State the blood parasite species.
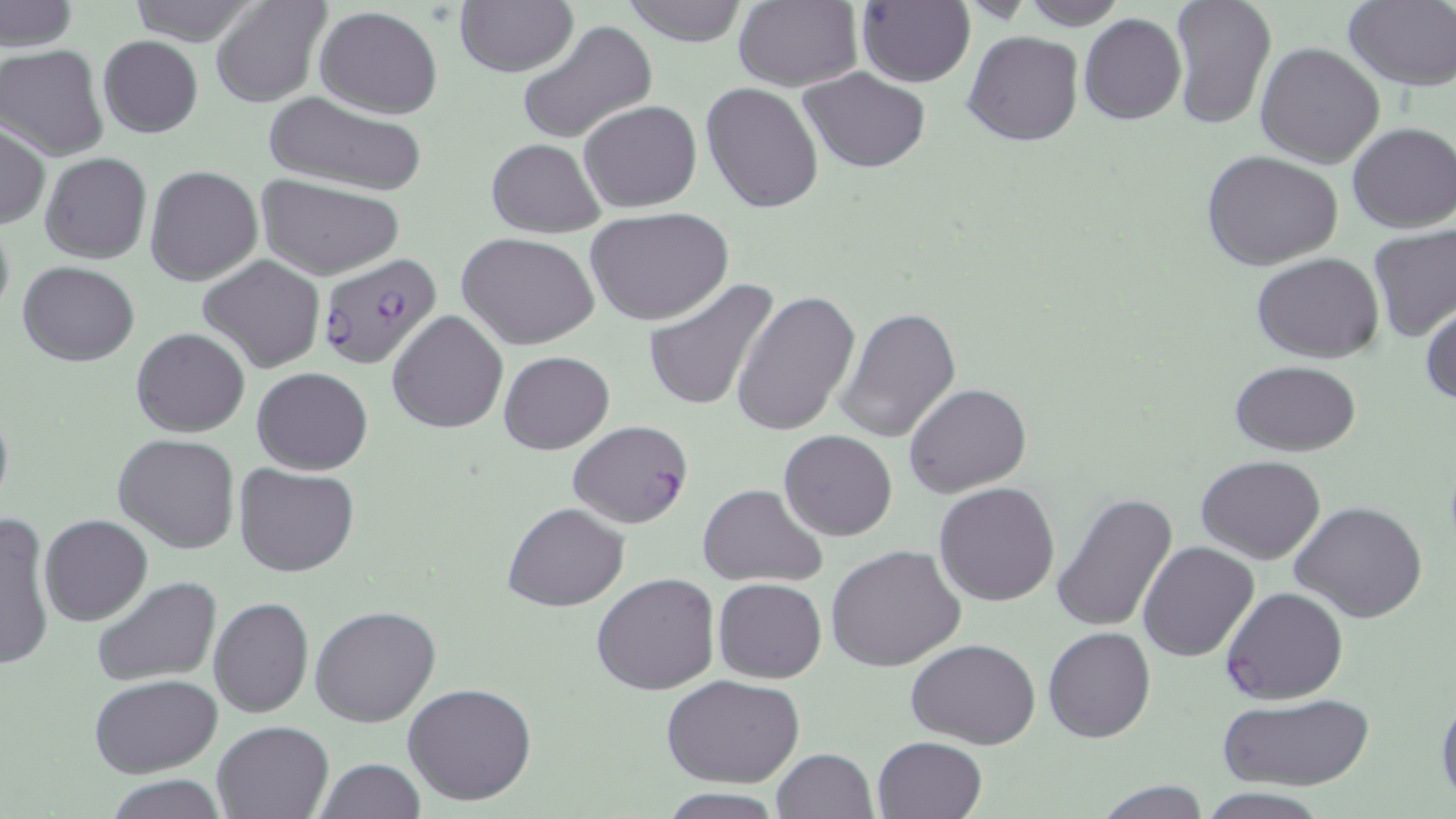

Plasmodium falciparum.

Summary:
  - Coordinate format: approximate bounding boxes as (x1,y1)-(x2,y2) corner pairs in pixels
  - Uninfected red blood cell locations: (0,0)-(76,52), (124,0)-(265,46), (212,0)-(331,108), (620,0)-(750,46), (732,0)-(861,92), (1017,0)-(1129,29), (1168,0)-(1277,130), (1343,1)-(1456,89), (454,2)-(577,77), (857,2)-(975,87), (314,5)-(443,118), (1078,13)-(1187,124), (516,20)-(659,146), (963,30)-(1084,147), (97,35)-(202,138), (1255,43)-(1385,168), (0,44)-(109,161), (798,68)-(931,173), (700,81)-(824,216), (262,91)-(428,196), (578,99)-(702,213), (0,122)-(50,229), (1346,123)-(1455,233), (487,138)-(605,237), (1199,149)-(1344,272), (40,152)-(151,264), (145,166)-(263,286), (257,174)-(405,279), (585,206)-(734,326), (0,213)-(14,325), (1367,226)-(1456,344), (459,234)-(599,350), (1251,252)-(1385,362), (199,256)-(325,372), (18,261)-(139,365), (643,277)-(780,415), (731,290)-(859,438), (1420,299)-(1455,408), (839,307)-(962,444), (386,310)-(508,432), (131,327)-(250,438), (499,351)-(614,453), (1230,359)-(1361,455), (251,367)-(374,475), (904,383)-(1031,498), (0,397)-(13,522), (778,428)-(898,542), (115,434)-(239,555), (1196,455)-(1326,564), (235,464)-(359,578), (935,481)-(1058,606), (697,482)-(828,588), (1051,493)-(1180,635), (1290,500)-(1427,623), (502,502)-(630,611), (0,512)-(55,673), (40,514)-(152,625), (1137,541)-(1258,662), (826,544)-(967,672), (591,571)-(720,696), (92,577)-(223,688), (713,578)-(826,683), (209,597)-(313,718), (309,606)-(441,728), (1043,627)-(1155,743), (905,639)-(1041,749), (90,674)-(220,777), (663,675)-(806,788), (403,682)-(538,806), (1434,689)-(1456,804), (1218,693)-(1373,790), (213,720)-(332,819), (872,735)-(987,819), (772,748)-(877,819), (314,759)-(425,818), (106,775)-(228,818), (1092,781)-(1215,818), (1196,788)-(1334,819), (657,789)-(787,819)
  - Plasmodium falciparum-infected red blood cell locations: (314,252)-(441,370), (568,420)-(693,528), (1220,586)-(1348,704)
  - Field of view: one of a larger specimen
  - Stain: May-Grünwald-Giemsa
  - Modality: light microscopy
  - Preparation: thin blood film
  - Image size: 1456×819 pixels
  - Magnification: 1000x